Identify the parasite.
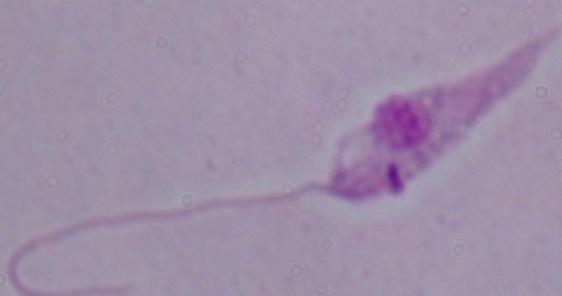
This is Leishmania.

Photomicrograph. Captured at 1000x magnification.